State which parasite is depicted.
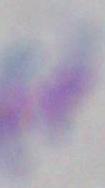

Toxoplasma gondii.

magnification: 1000x
modality: micrograph